Identify the parasite.
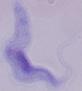

A trypanosome.

1000x magnification. Micrograph.